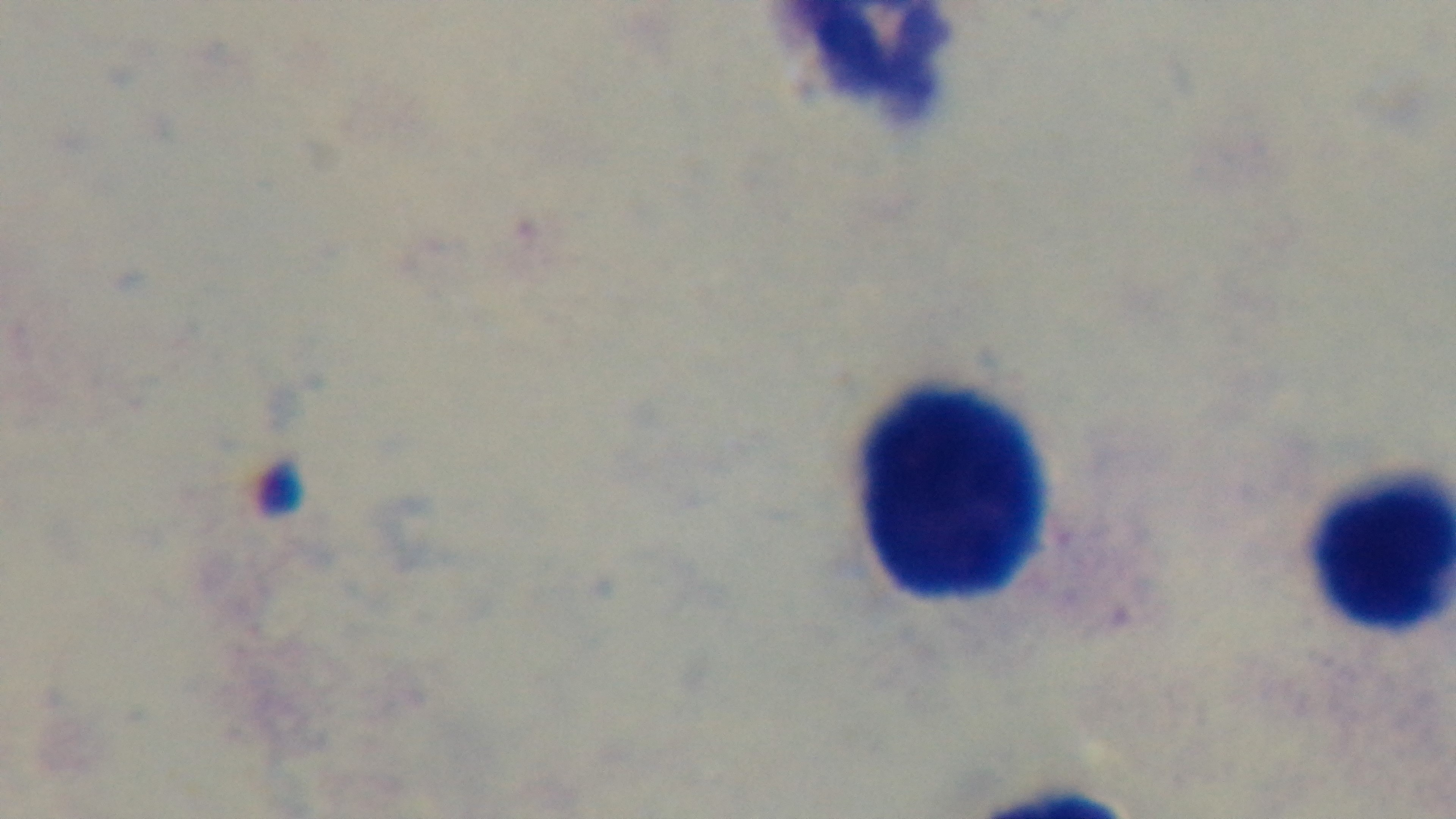

Single field of view. Oil-immersion objective, 100x. Malaria status: negative. Light microscopy. Giemsa-stained. Preparation: thick blood film. Mounted 4K digital camera.